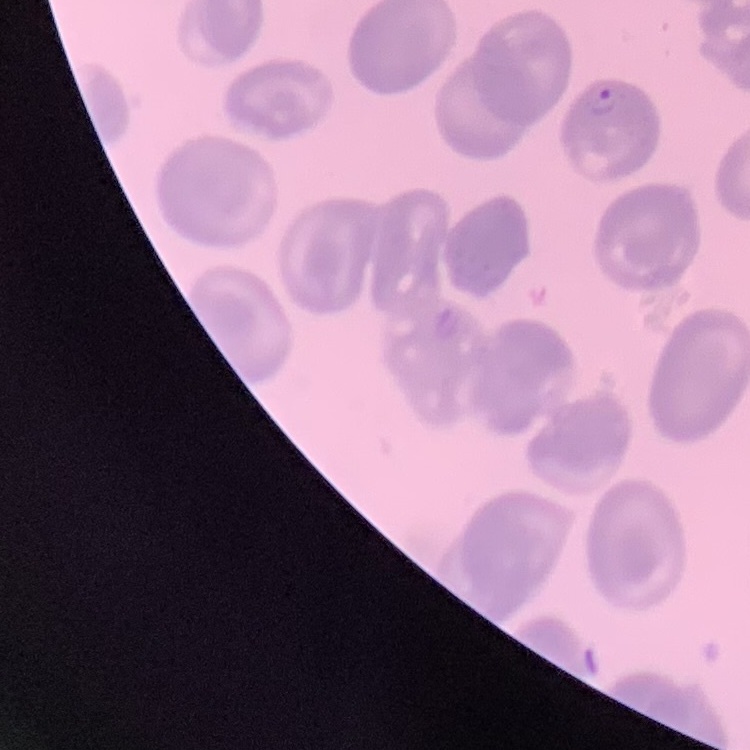
Summary:
  - Erythrocyte morphology: no rouleaux formation
  - Preparation: thin blood smear
  - Stain: Field's or Giemsa
  - Image type: one tile cut from a larger photomicrograph